Report the malaria status of this cell.
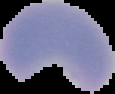

It is parasitized.

Summary:
  - Preparation: thin blood smear
  - Image type: cell region segmented out of the field of view; surrounding area masked to black
  - Image size: 115×94 pixels